Assess for malaria.
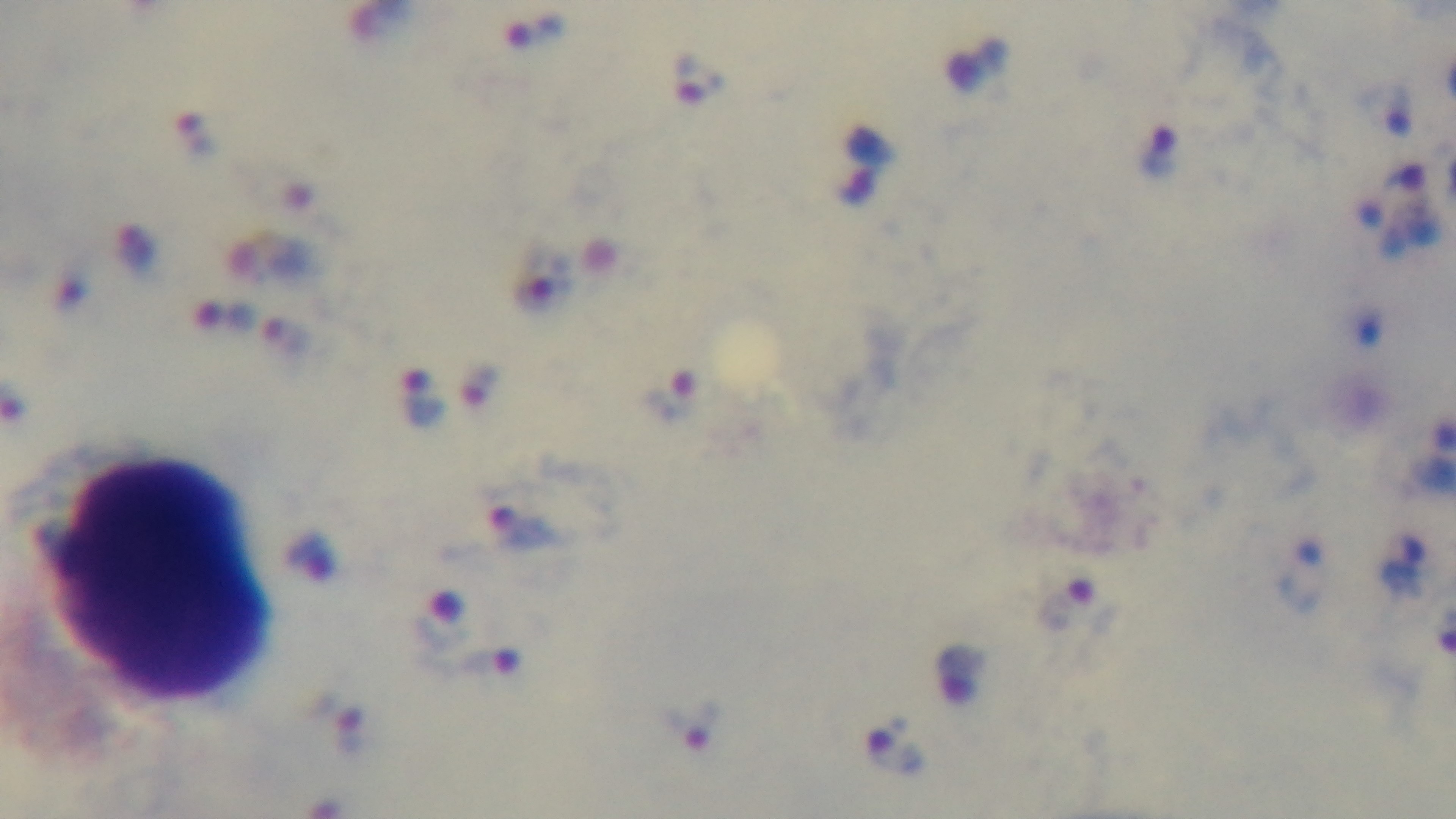

Positive.

Preparation: thick. Giemsa stain. Captured with a mounted 4K digital camera. Single field of view. Photomicrograph. Oil-immersion objective, 100x.